Classify this cell by malaria status.
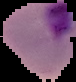
It is parasitized.

Cell region segmented out of the field of view; the surrounding area is masked to black. From a thin blood film. Image is 76×82 pixels.